Identify the preparation type.
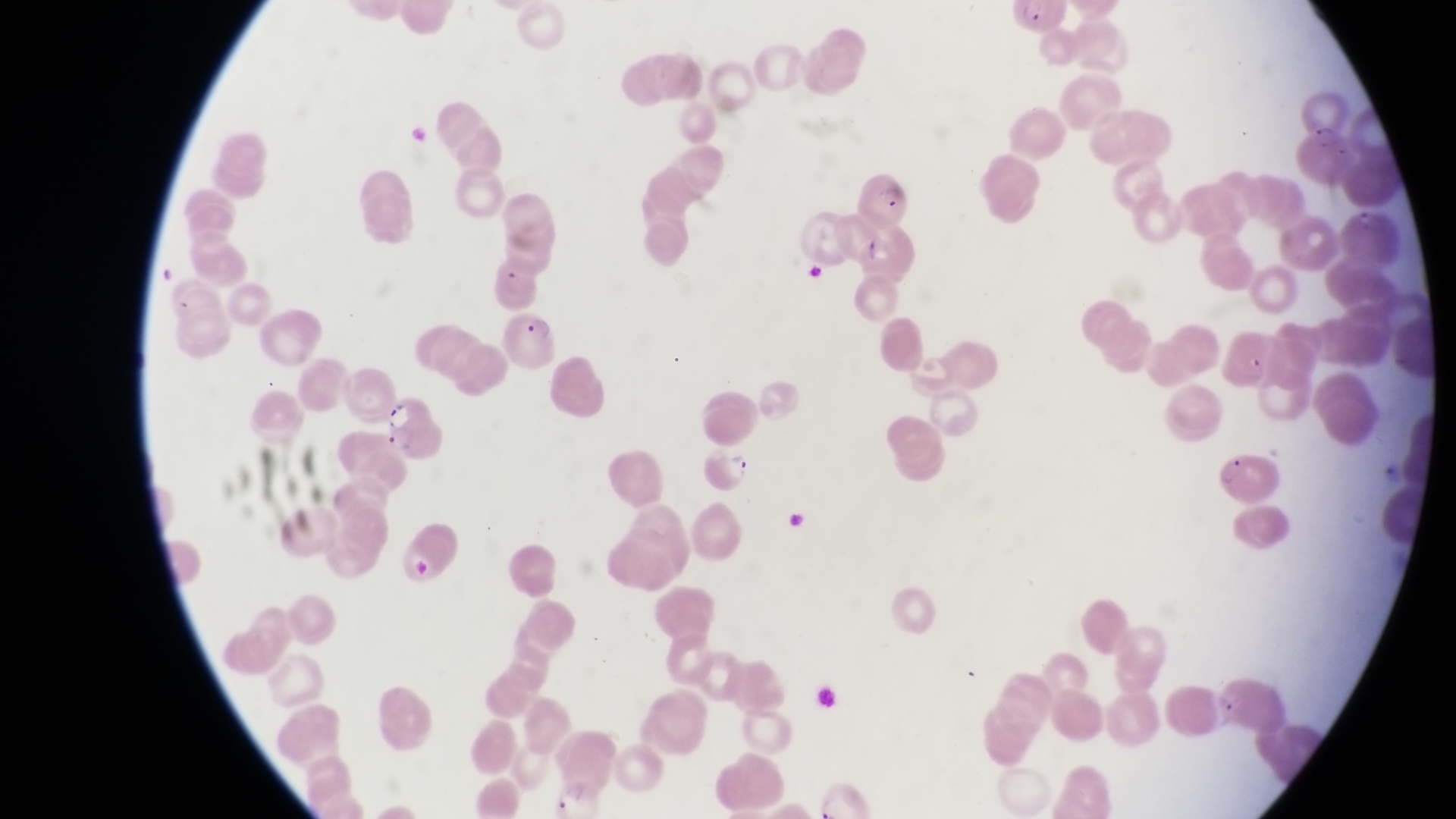
This is a thin smear.

Approximate bounding boxes as [left, top, right, bottom] in pixels.
Summary:
  - Trophozoite locations: [555, 779, 592, 815]
  - Parasitised red blood cell locations: [1297, 80, 1353, 152], [855, 174, 905, 226], [507, 307, 567, 379], [381, 393, 447, 460], [703, 446, 755, 493], [1216, 446, 1280, 496]
  - Field of view: single
  - Magnification: 1000x
  - Capture: smartphone photograph through the eyepiece of an Olympus CX-23 microscope
  - Image size: 1456×819 pixels
  - Country: Uganda